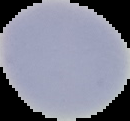 Image is 130×121 pixels. From a thin blood smear. Cell region segmented out of the field of view; the surrounding area is masked to black. Result: no malaria parasites detected.